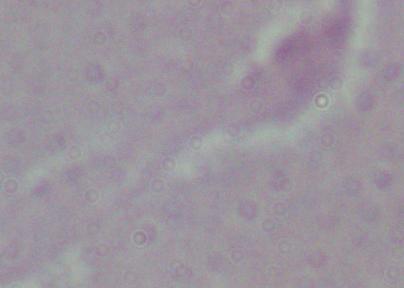

identification = Leishmania
magnification = 1000x
modality = photomicrograph